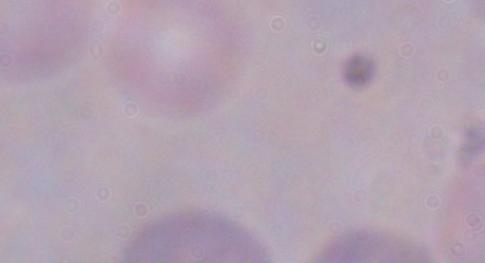
Summary:
  - Modality: micrograph
  - Magnification: 1000x
  - Identification: trypanosome